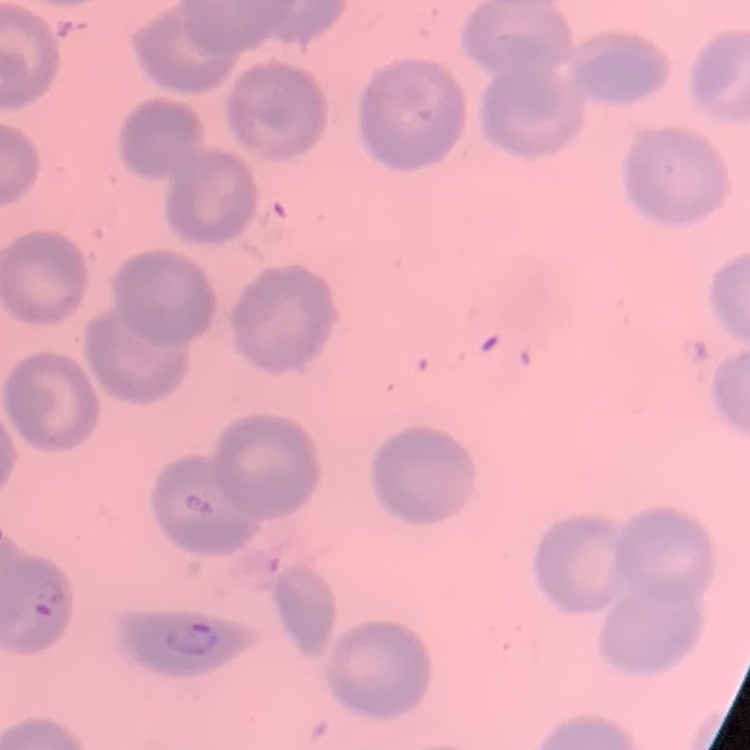 The erythrocytes show no rouleaux formation. Field's or Giemsa stain. Thin blood smear. Square crop of a larger photomicrograph.